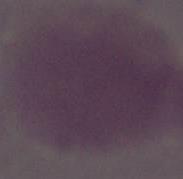
Summary:
  - Modality: micrograph
  - Magnification: 1000x
  - Identification: red blood cell